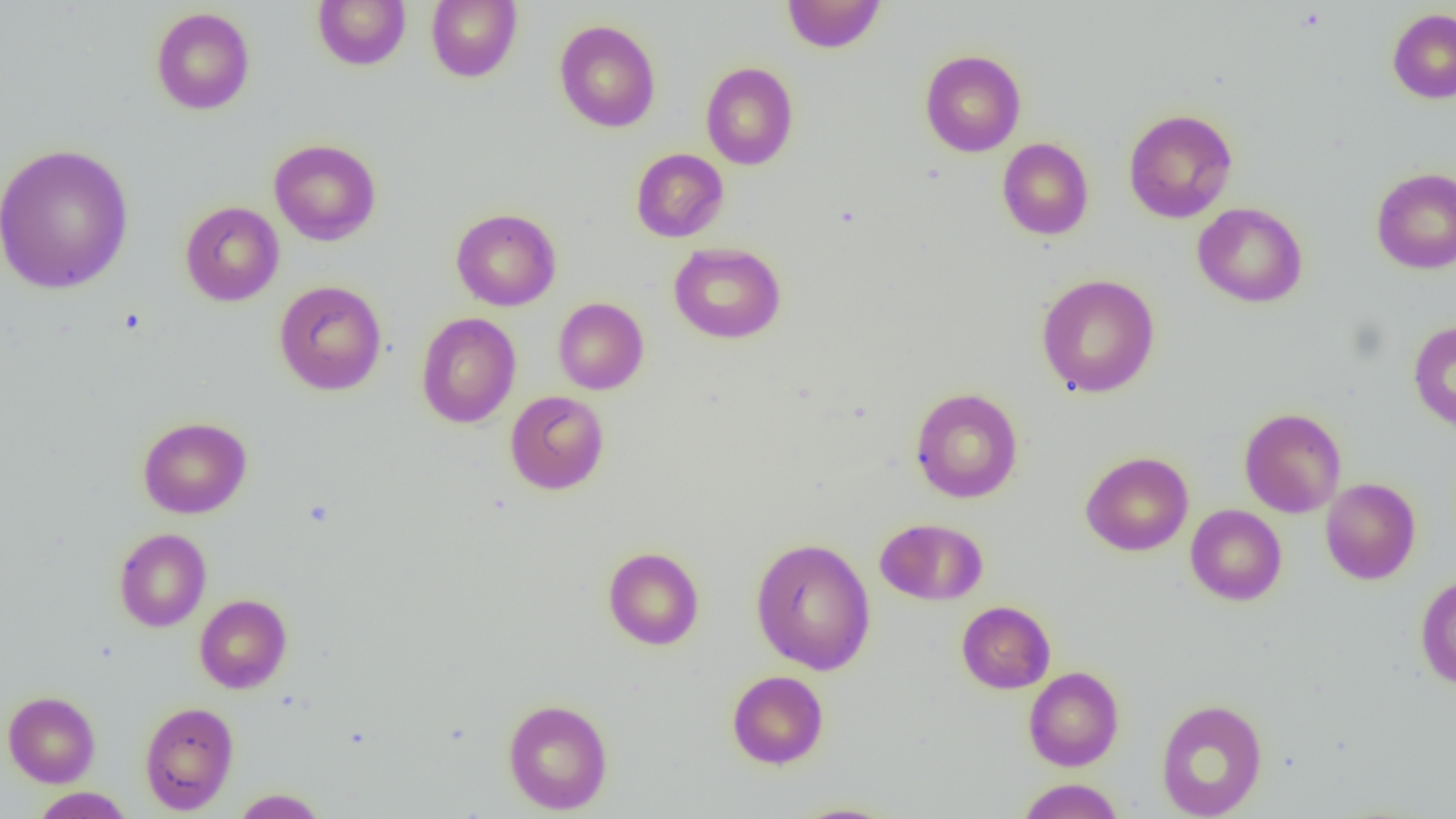

slide-level diagnosis = negative for blood parasites
preparation = thin blood film
image size = 1456×819 pixels
modality = optical microscopy
field of view = single
magnification = 1000x
uninfected red blood cell locations = approximate bounding boxes as named x1/y1/x2/y2 corners in pixels: (x1=312, y1=0, x2=410, y2=70), (x1=426, y1=0, x2=522, y2=82), (x1=782, y1=0, x2=887, y2=53), (x1=150, y1=7, x2=255, y2=115), (x1=1387, y1=9, x2=1456, y2=103), (x1=554, y1=19, x2=661, y2=133), (x1=920, y1=49, x2=1026, y2=157), (x1=700, y1=62, x2=799, y2=169), (x1=1123, y1=108, x2=1237, y2=223), (x1=997, y1=138, x2=1094, y2=239), (x1=269, y1=139, x2=381, y2=245), (x1=0, y1=142, x2=134, y2=296), (x1=631, y1=148, x2=729, y2=242), (x1=1371, y1=167, x2=1456, y2=274), (x1=179, y1=201, x2=284, y2=306), (x1=1192, y1=202, x2=1308, y2=307), (x1=451, y1=208, x2=561, y2=311), (x1=669, y1=242, x2=786, y2=344), (x1=1035, y1=273, x2=1161, y2=398), (x1=274, y1=280, x2=387, y2=395), (x1=553, y1=297, x2=649, y2=395), (x1=416, y1=312, x2=521, y2=428), (x1=1408, y1=320, x2=1456, y2=431), (x1=910, y1=387, x2=1023, y2=503), (x1=505, y1=390, x2=610, y2=495), (x1=1239, y1=407, x2=1346, y2=518), (x1=138, y1=416, x2=252, y2=518), (x1=1080, y1=451, x2=1193, y2=556), (x1=1320, y1=478, x2=1421, y2=584), (x1=1186, y1=504, x2=1287, y2=605), (x1=875, y1=518, x2=987, y2=605), (x1=113, y1=528, x2=212, y2=632), (x1=750, y1=537, x2=876, y2=675), (x1=603, y1=546, x2=704, y2=650), (x1=1415, y1=574, x2=1456, y2=690), (x1=194, y1=594, x2=292, y2=693), (x1=956, y1=600, x2=1055, y2=693), (x1=1023, y1=666, x2=1124, y2=771), (x1=726, y1=670, x2=829, y2=769), (x1=3, y1=691, x2=100, y2=787), (x1=502, y1=698, x2=613, y2=814), (x1=1155, y1=698, x2=1268, y2=819), (x1=139, y1=701, x2=239, y2=813), (x1=1016, y1=778, x2=1126, y2=819), (x1=31, y1=787, x2=134, y2=818), (x1=230, y1=788, x2=329, y2=818), (x1=787, y1=802, x2=904, y2=819)